Describe the morphology of the erythrocytes.
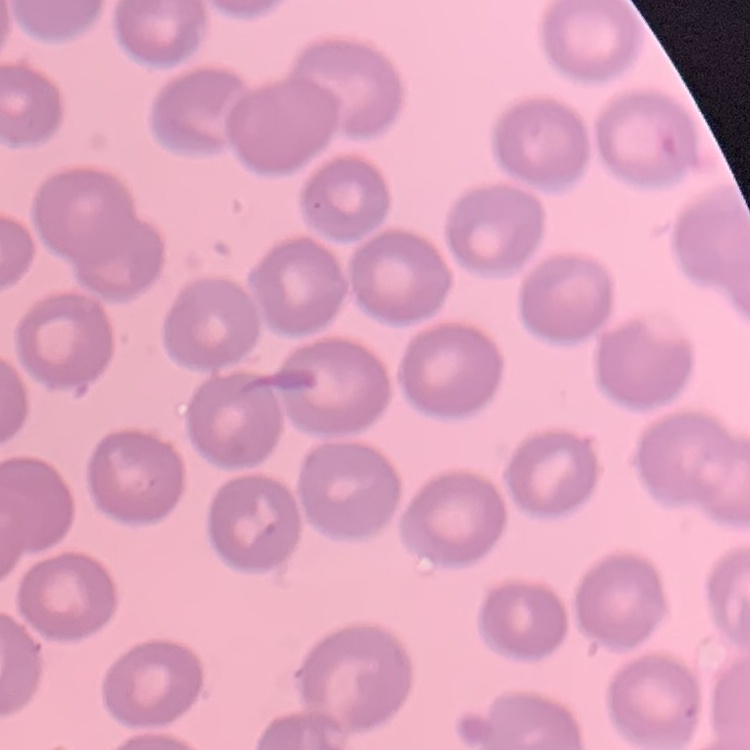

No rouleaux formation.

Summary:
  - Stain: Field's or Giemsa
  - Preparation: thin blood film
  - Image type: one tile cut from a larger photomicrograph